Assess the morphology of the erythrocytes.
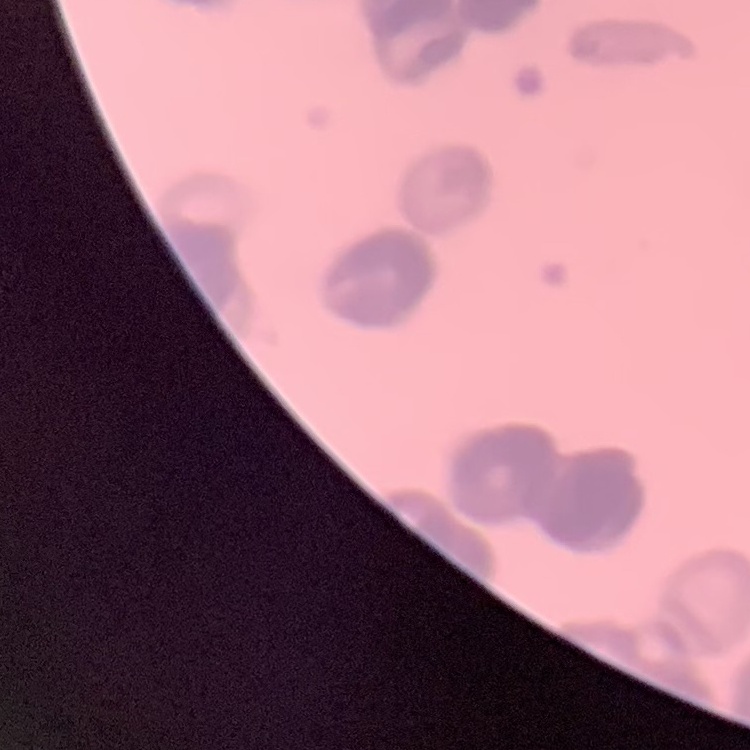
They show rouleaux formation.

One tile cut from a larger photomicrograph. Stained with either Field's or Giemsa. Thin peripheral smear.